Assess this cell for malaria.
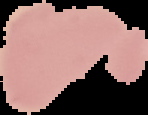

Uninfected.

Cell region segmented out of the field of view; the surrounding area is masked to black. From a thin blood film. Image is 148×115 pixels.